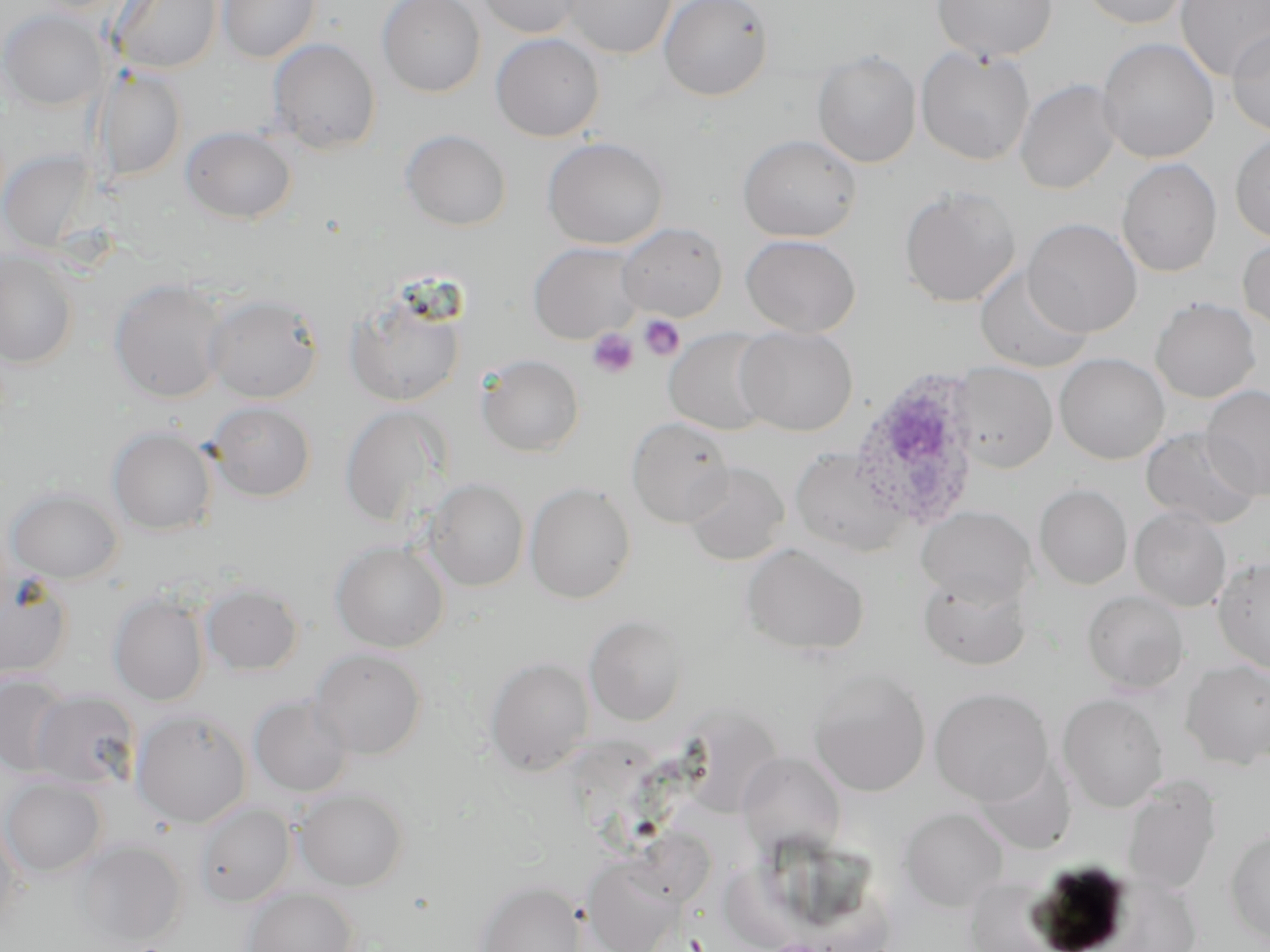

{
  "slide_level_diagnosis": "Plasmodium ovale",
  "modality": "light microscopy",
  "preparation": "thin blood smear",
  "field_of_view": "single",
  "plasmodium_ovale_infected_red_blood_cell_locations": "approximate bounding boxes as (x1,y1)-(x2,y2) corner pairs in pixels: (848,367)-(984,531)",
  "magnification": "1000x",
  "image_size": "1270×952 pixels",
  "uninfected_red_blood_cell_locations": "approximate bounding boxes as (x1,y1)-(x2,y2) corner pairs in pixels: (111,0)-(223,73), (377,0)-(485,97), (474,0)-(587,38), (562,0)-(678,59), (658,0)-(773,100), (932,0)-(1058,62), (1077,0)-(1194,30), (1175,0)-(1270,82), (217,1)-(321,63), (1,8)-(107,111), (1226,28)-(1270,137), (490,33)-(605,142), (1096,37)-(1219,164), (267,38)-(381,154), (915,46)-(1035,166), (812,49)-(922,168), (94,68)-(187,182), (1015,79)-(1122,195), (181,126)-(296,223), (400,129)-(511,231), (1230,131)-(1270,244), (737,134)-(863,242), (541,136)-(670,250), (1,149)-(97,252), (1117,158)-(1222,277), (898,185)-(1021,307), (1022,218)-(1142,337), (616,222)-(727,322), (740,234)-(860,337), (1237,235)-(1270,335), (528,241)-(645,343), (0,252)-(79,368), (974,263)-(1093,373), (109,278)-(230,403), (345,286)-(468,408), (203,292)-(324,403), (1150,297)-(1261,403), (735,326)-(858,436), (664,328)-(776,436), (1054,353)-(1169,464), (476,354)-(584,457), (950,362)-(1057,474), (1202,384)-(1270,500), (206,401)-(316,501), (339,405)-(452,529), (626,416)-(734,528), (108,426)-(217,535), (1140,427)-(1263,531), (790,446)-(912,557), (683,461)-(789,565), (424,478)-(529,591), (525,482)-(637,604), (1034,484)-(1133,589), (6,486)-(123,583), (916,506)-(1036,605), (1129,507)-(1232,612), (331,541)-(449,652), (740,542)-(870,657), (1213,556)-(1270,675), (0,566)-(73,682), (918,570)-(1032,671), (200,582)-(303,676), (1082,589)-(1189,693), (108,592)-(210,706), (584,614)-(688,726), (309,648)-(427,759), (484,657)-(595,776), (1181,660)-(1270,770), (807,667)-(930,797), (0,673)-(73,776), (930,687)-(1053,805), (29,690)-(140,789), (1058,693)-(1169,811), (248,695)-(354,798), (131,708)-(252,828), (737,752)-(846,855), (974,755)-(1077,854), (1119,775)-(1221,897), (1,778)-(107,878), (294,787)-(409,891), (193,802)-(296,907), (900,807)-(1008,911), (0,816)-(24,933), (1225,826)-(1270,946), (76,840)-(186,948), (582,853)-(686,951), (476,879)-(586,952), (242,887)-(359,951)",
  "stain": "May-Grünwald-Giemsa",
  "platelet_locations": "approximate bounding boxes as (x1,y1)-(x2,y2) corner pairs in pixels: (638,314)-(685,361), (588,327)-(640,379)"
}